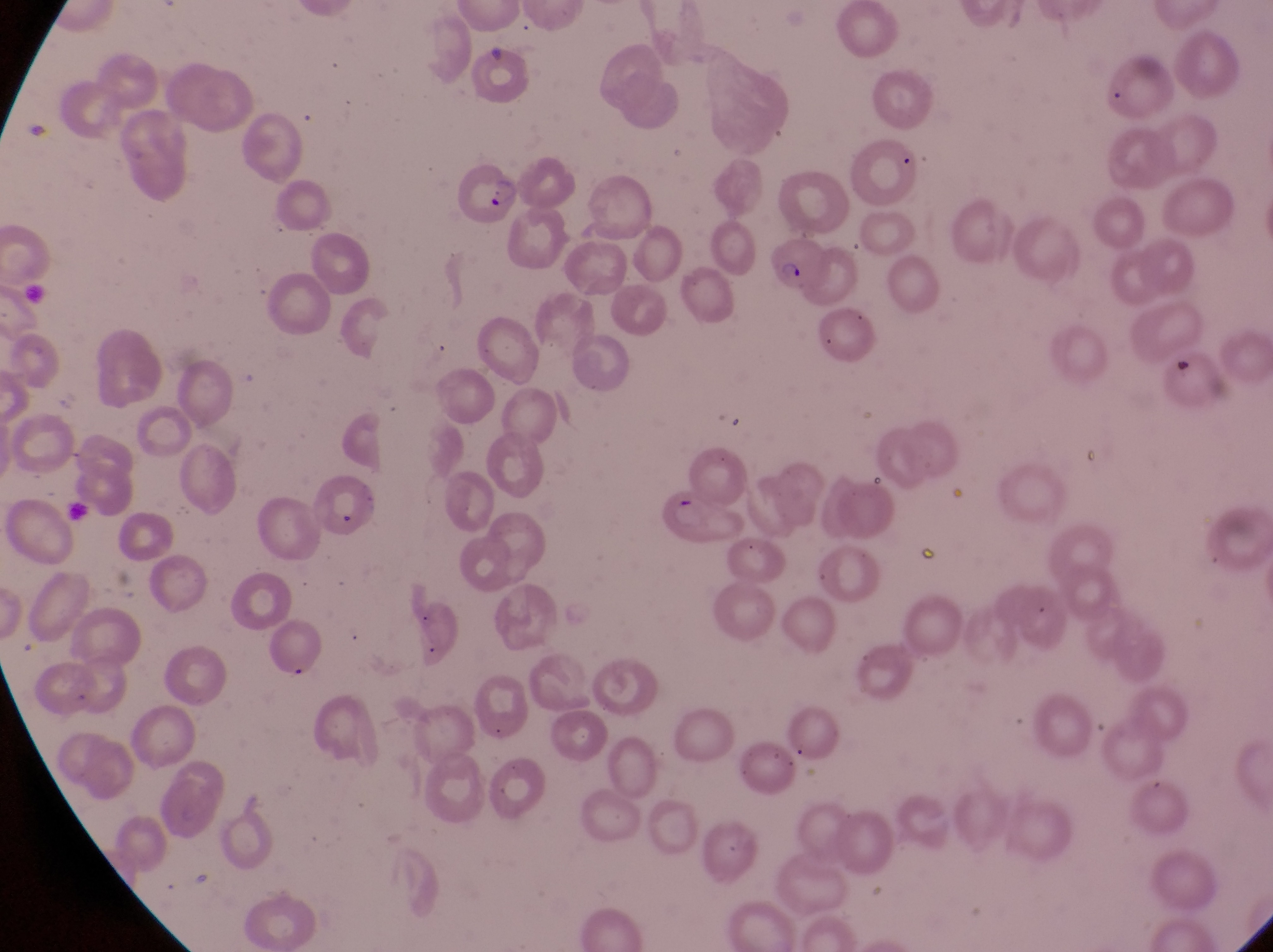

Approximate bounding boxes as (left, top, right, bottom) in pixels.
Summary:
  - Parasitised red blood cell locations: (454, 157, 526, 231), (771, 235, 829, 292), (309, 477, 381, 542), (661, 491, 743, 546)
  - Preparation: thin blood smear
  - Country: Uganda
  - Image size: 1273×952 pixels
  - Field of view: single
  - Capture: smartphone photograph through the eyepiece of an Olympus CX-23 microscope
  - Magnification: 1000x